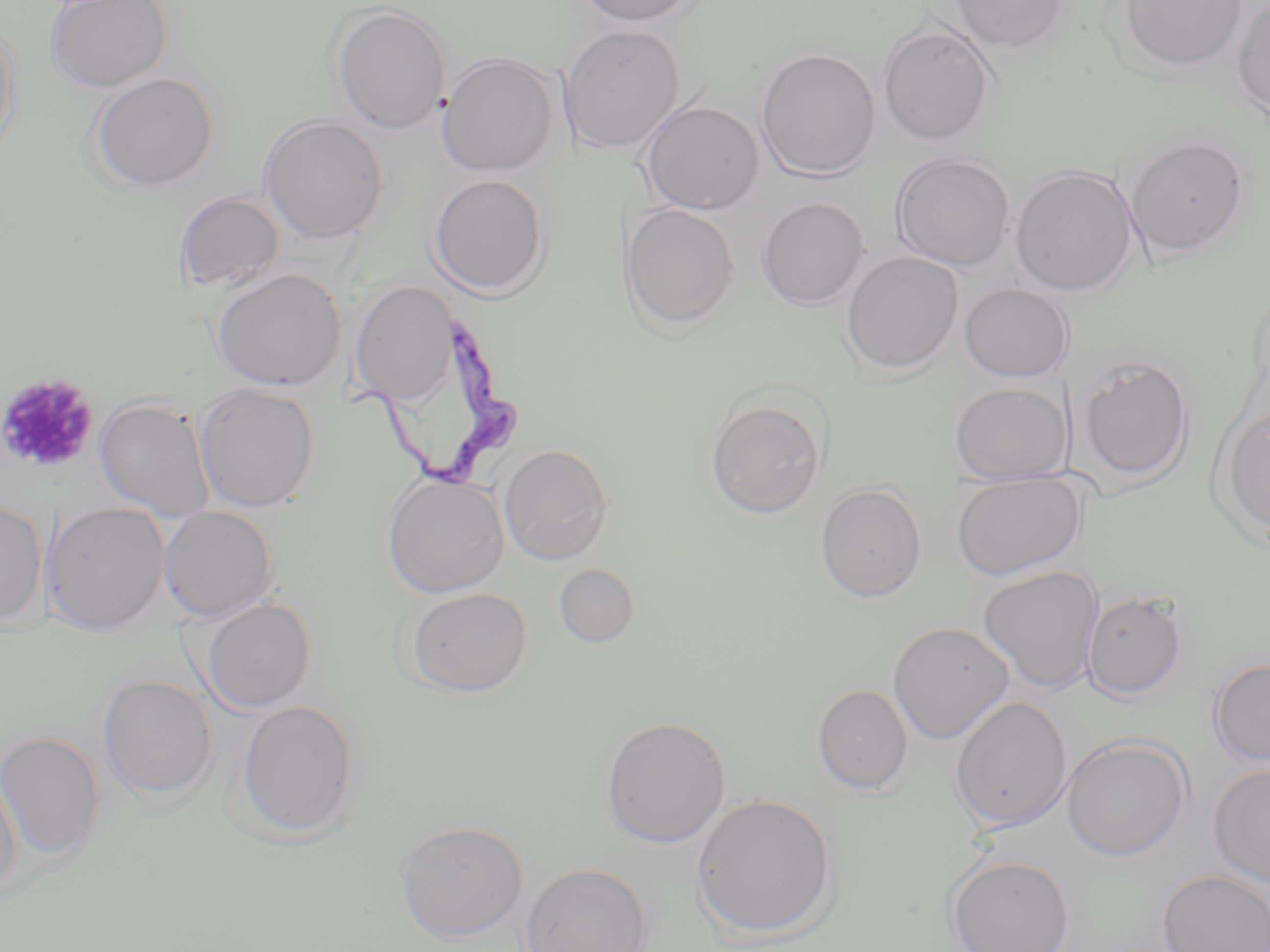 Approximate bounding boxes as named x1/y1/x2/y2 corners in pixels. Uninfected red blood cell locations: (x1=45, y1=0, x2=172, y2=93), (x1=576, y1=0, x2=703, y2=27), (x1=950, y1=0, x2=1069, y2=53), (x1=1116, y1=0, x2=1247, y2=75), (x1=1231, y1=0, x2=1270, y2=122), (x1=331, y1=3, x2=452, y2=134), (x1=877, y1=22, x2=998, y2=146), (x1=559, y1=24, x2=685, y2=155), (x1=0, y1=25, x2=20, y2=153), (x1=755, y1=47, x2=881, y2=182), (x1=436, y1=52, x2=561, y2=178), (x1=87, y1=71, x2=219, y2=193), (x1=640, y1=99, x2=764, y2=215), (x1=259, y1=114, x2=389, y2=244), (x1=1123, y1=134, x2=1250, y2=261), (x1=889, y1=152, x2=1016, y2=272), (x1=1010, y1=165, x2=1140, y2=297), (x1=428, y1=173, x2=551, y2=299), (x1=174, y1=191, x2=285, y2=295), (x1=757, y1=196, x2=870, y2=310), (x1=620, y1=202, x2=741, y2=333), (x1=841, y1=251, x2=963, y2=375), (x1=211, y1=268, x2=347, y2=392), (x1=350, y1=281, x2=459, y2=407), (x1=960, y1=284, x2=1073, y2=382), (x1=1077, y1=353, x2=1195, y2=485), (x1=194, y1=382, x2=320, y2=513), (x1=949, y1=382, x2=1073, y2=485), (x1=94, y1=397, x2=216, y2=520), (x1=706, y1=397, x2=828, y2=519), (x1=1215, y1=401, x2=1270, y2=542), (x1=498, y1=444, x2=614, y2=566), (x1=951, y1=472, x2=1086, y2=580), (x1=381, y1=473, x2=509, y2=598), (x1=815, y1=482, x2=927, y2=603), (x1=0, y1=500, x2=49, y2=629), (x1=42, y1=501, x2=170, y2=635), (x1=159, y1=506, x2=278, y2=622), (x1=554, y1=563, x2=639, y2=648), (x1=978, y1=566, x2=1104, y2=693), (x1=406, y1=587, x2=533, y2=696), (x1=1082, y1=588, x2=1190, y2=701), (x1=199, y1=598, x2=316, y2=713), (x1=888, y1=620, x2=1015, y2=743), (x1=1208, y1=657, x2=1270, y2=765), (x1=98, y1=675, x2=219, y2=804), (x1=812, y1=684, x2=913, y2=795), (x1=949, y1=695, x2=1073, y2=833), (x1=235, y1=698, x2=361, y2=843), (x1=600, y1=715, x2=731, y2=849), (x1=0, y1=731, x2=105, y2=861), (x1=1061, y1=733, x2=1192, y2=861), (x1=1207, y1=763, x2=1270, y2=888), (x1=0, y1=770, x2=23, y2=904), (x1=692, y1=793, x2=839, y2=942), (x1=393, y1=819, x2=528, y2=943), (x1=944, y1=854, x2=1075, y2=952), (x1=519, y1=862, x2=653, y2=952), (x1=1156, y1=870, x2=1270, y2=952). Platelet locations: (x1=0, y1=372, x2=99, y2=473). Trypanosoma brucei locations: (x1=343, y1=313, x2=526, y2=505). Slide-level diagnosis: Trypanosoma brucei. May-Grünwald-Giemsa stain. One field of a larger specimen. Thin blood smear. Light microscopy. 1000x magnification. Image is 1270×952 pixels.